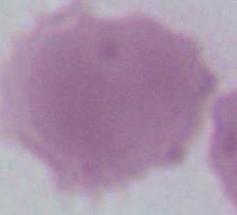 Micrograph. 1000x magnification. An erythrocyte is seen.